Comment on the morphology of the red blood cells.
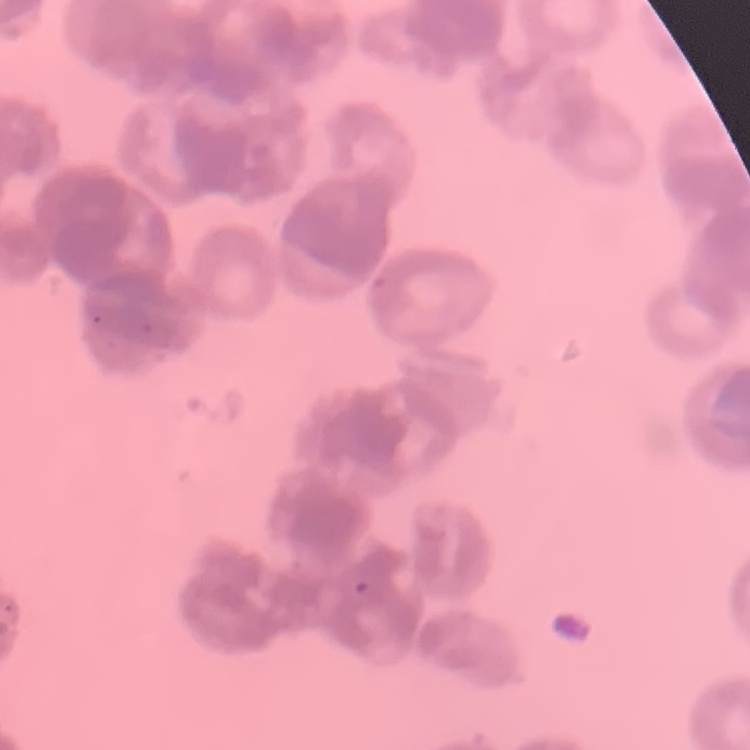

Rouleaux formation.

image type = one tile cut from a larger photomicrograph
preparation = thin blood film
stain = Field's or Giemsa